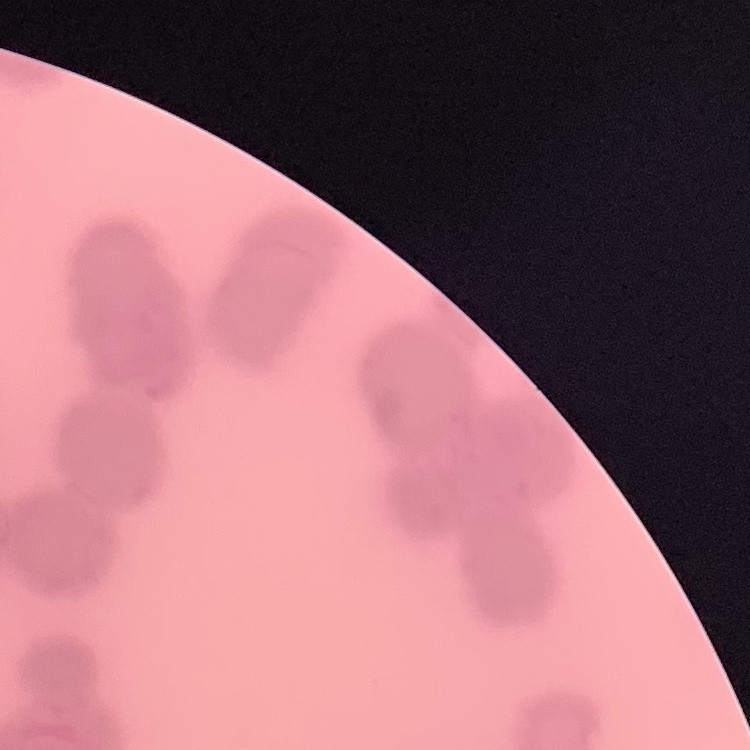
erythrocyte morphology = rouleaux formation
preparation = thin blood smear
stain = Field's or Giemsa
image type = square crop of a larger photomicrograph